Name the cell type shown.
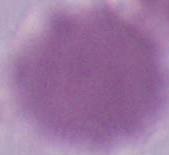
This is an erythrocyte.

modality = photomicrograph
magnification = 1000x